State which cell type is depicted.
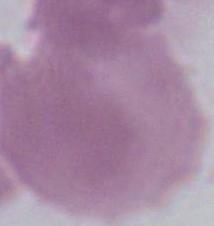
An erythrocyte.

{
  "modality": "micrograph",
  "magnification": "1000x"
}